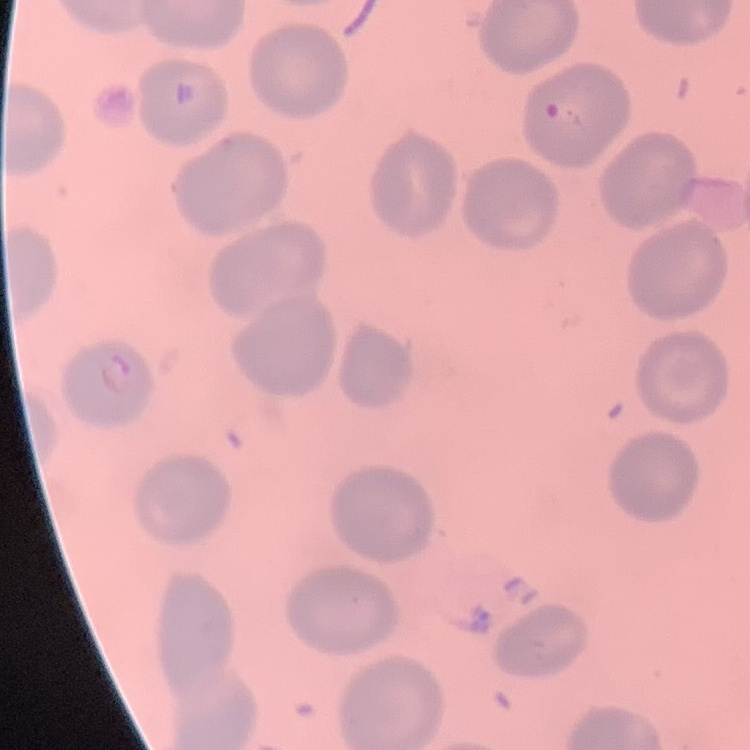

The red blood cells exhibit no rouleaux formation. Field's or Giemsa stain. One tile cut from a larger photomicrograph. Thin peripheral smear.